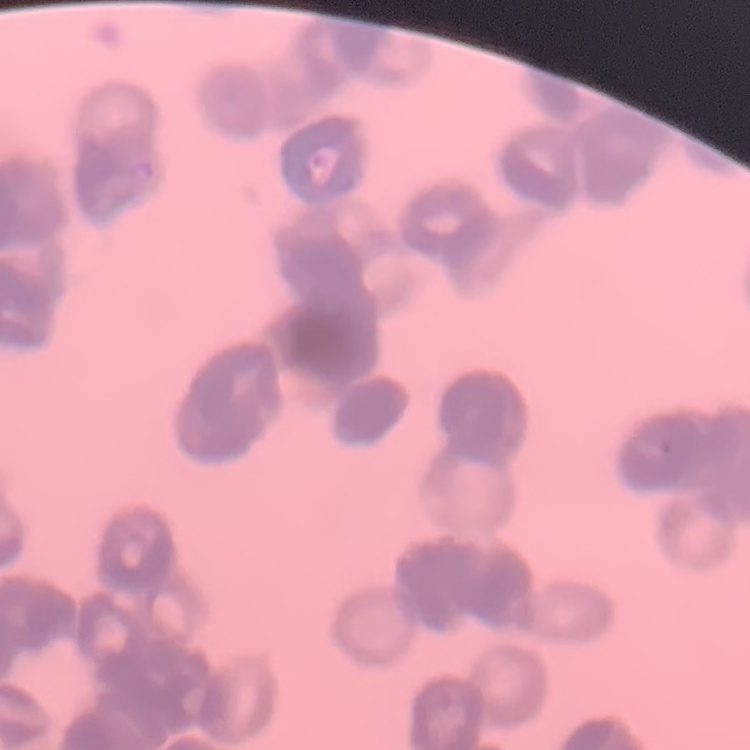
The erythrocytes show rouleaux formation. Square crop of a larger photomicrograph. Field's or Giemsa stain. Thin blood film.